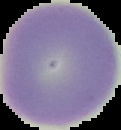
{
  "image_type": "segmented cell region with the area outside set to black",
  "preparation": "thin blood film",
  "image_size": "121×130 pixels",
  "result": "negative for Plasmodium parasites"
}